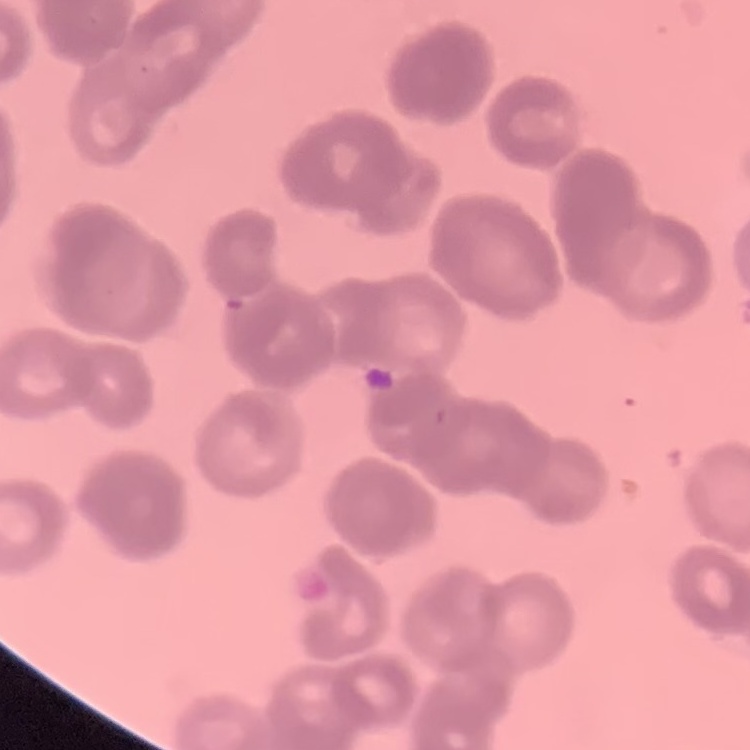
The red blood cells show rouleaux formation. Square crop of a larger photomicrograph. Stained with either Field's or Giemsa. Thin peripheral smear.